Report the malaria status of this cell.
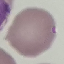
Uninfected.

Summary:
  - Image type: cell patch, automatically extracted from a larger field of view and resized to 64 × 64 pixels
  - Stain: Giemsa
  - Capture: smartphone through the microscope eyepiece
  - Preparation: thin blood smear